Name the parasite shown.
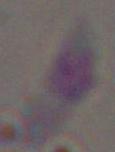
Toxoplasma gondii.

modality: photomicrograph
magnification: 1000x